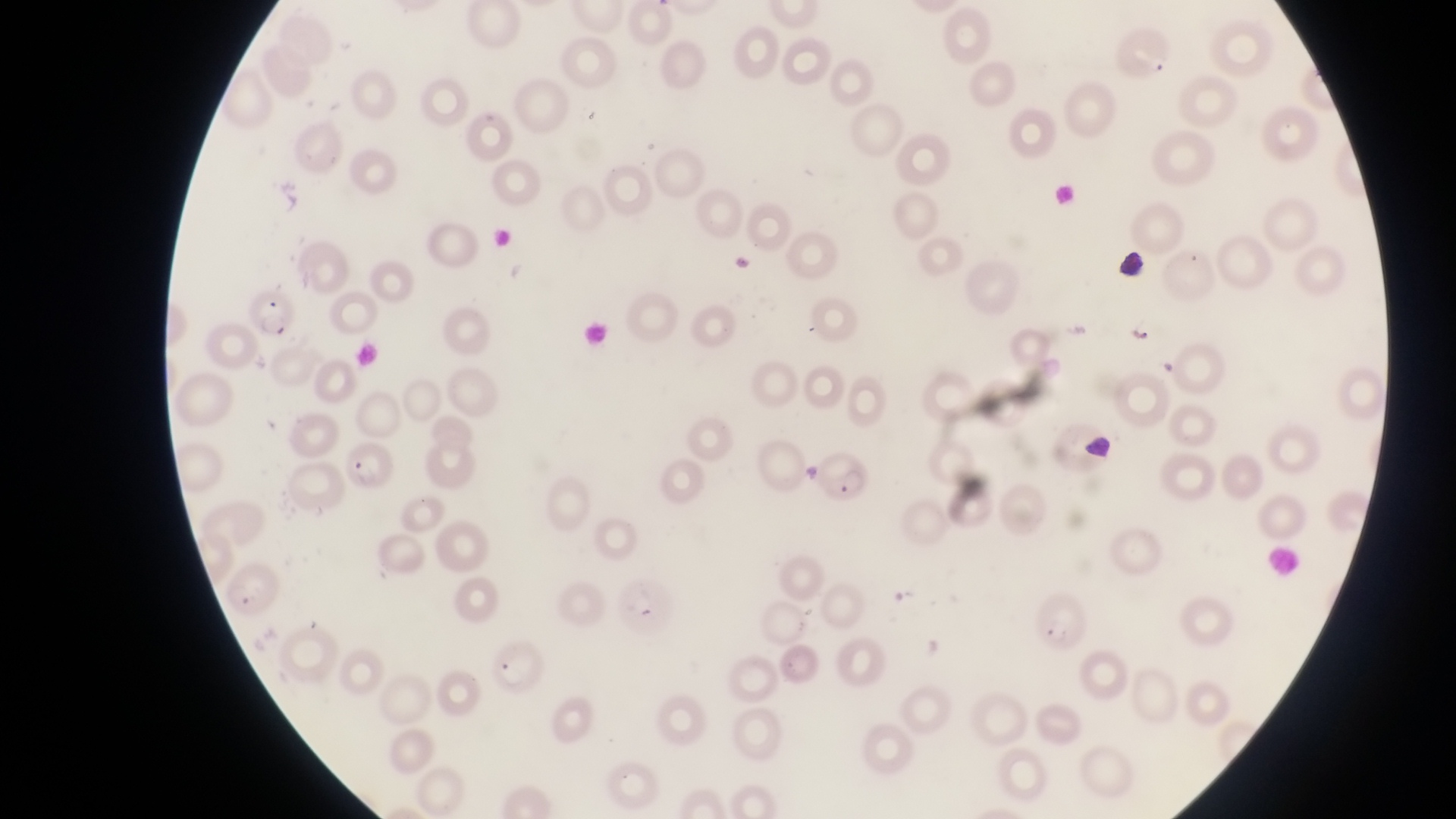 Approximate bounding boxes as (left, top, right, bottom) in pixels. Object labeled both parasitised red blood cell and trophozoite by the source: (1133, 315, 1162, 347). Leukocyte locations: (1112, 246, 1149, 282), (1081, 431, 1112, 464). Parasitised red blood cell locations: (243, 293, 303, 342), (346, 439, 401, 491), (817, 446, 878, 507), (613, 576, 679, 637), (1031, 592, 1091, 652), (489, 637, 547, 697). Collected in Uganda. Thin blood film. At a magnification of 1000x. Photographed through the eyepiece of an Olympus CX-23 microscope with a smartphone camera. Image is 1456×819 pixels. One field of view.